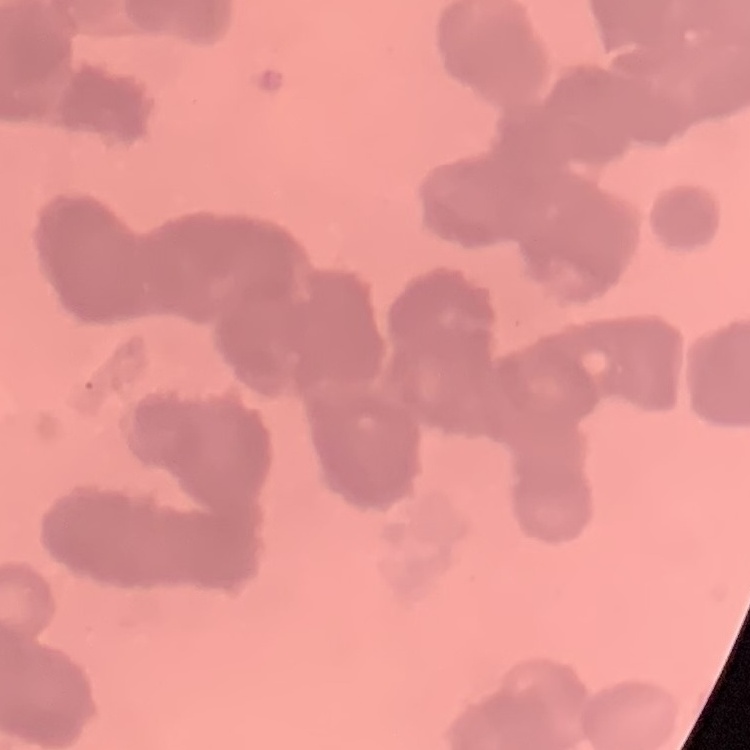

Summary:
  - Erythrocyte morphology: rouleaux formation
  - Stain: Field's or Giemsa
  - Image type: square crop of a larger photomicrograph
  - Preparation: thin peripheral smear